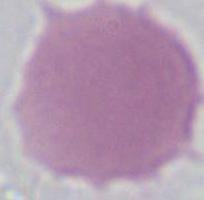
Summary:
  - Modality: photomicrograph
  - Identification: erythrocyte
  - Magnification: 1000x